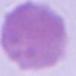
{
  "magnification": "1000x",
  "identification": "red blood cell",
  "modality": "micrograph"
}